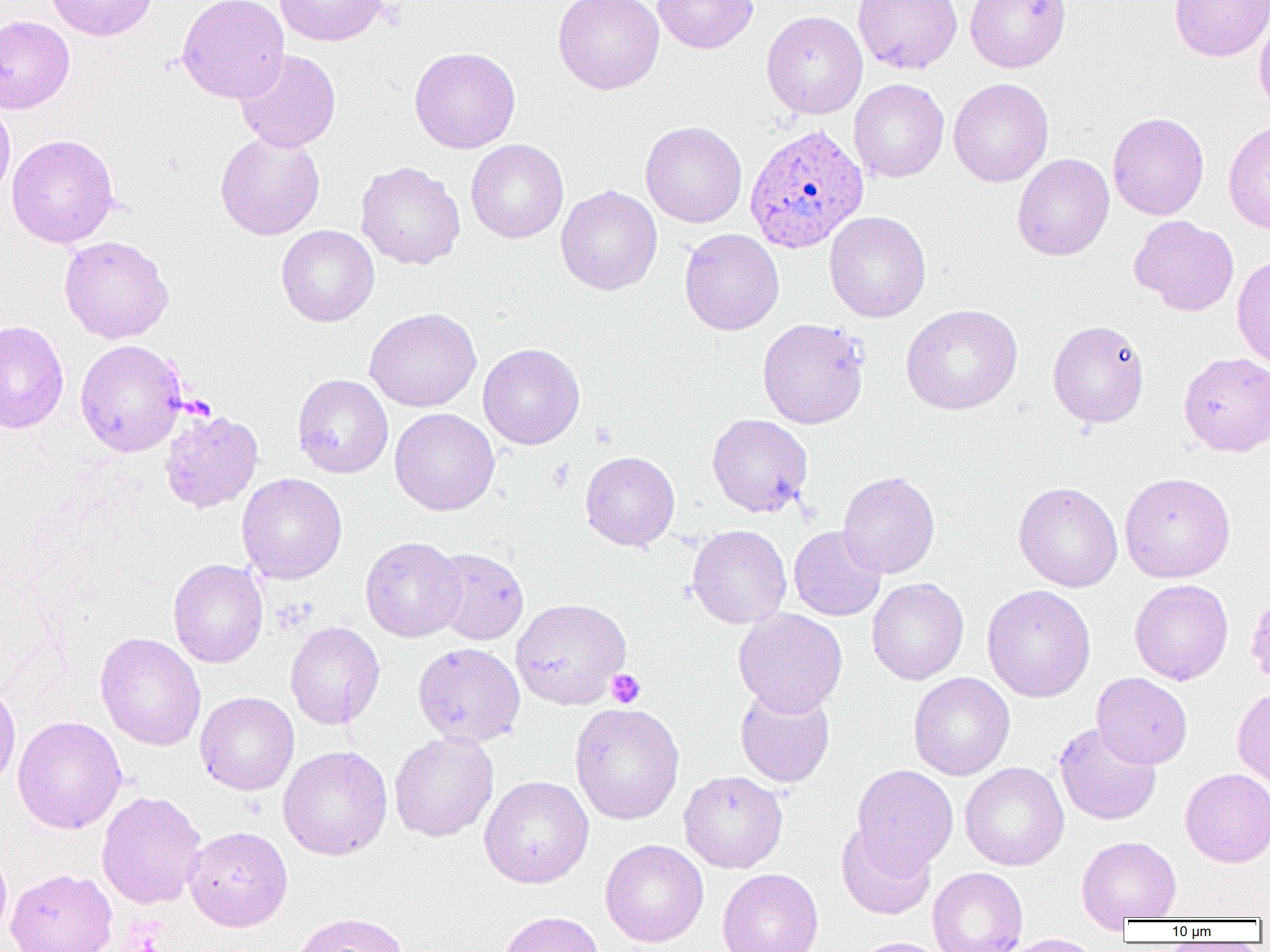
Summary:
  - Coordinate format: approximate bounding boxes as (x1, y1, x2, y2) in pixels
  - Plasmodium ovale-infected red blood cell locations: (743, 123, 869, 253)
  - Uninfected red blood cell locations: (45, 0, 158, 41), (177, 0, 290, 103), (275, 0, 387, 47), (553, 0, 664, 94), (652, 0, 758, 54), (853, 0, 962, 74), (964, 0, 1071, 72), (1169, 1, 1270, 62), (1254, 7, 1270, 118), (761, 10, 868, 118), (0, 15, 75, 113), (409, 46, 521, 153), (235, 49, 341, 152), (948, 77, 1054, 187), (849, 78, 949, 183), (0, 97, 15, 205), (1107, 112, 1209, 220), (1223, 120, 1270, 234), (640, 121, 747, 228), (215, 132, 325, 241), (7, 134, 119, 247), (466, 139, 568, 243), (1012, 153, 1114, 261), (355, 160, 465, 270), (556, 185, 662, 295), (824, 211, 931, 322), (1129, 215, 1239, 316), (276, 224, 379, 327), (679, 228, 784, 335), (59, 235, 174, 343), (1232, 254, 1270, 370), (900, 303, 1023, 414), (364, 307, 482, 412), (757, 317, 870, 429), (1047, 319, 1150, 428), (0, 320, 69, 433), (75, 339, 187, 457), (478, 343, 585, 449), (1179, 351, 1269, 456), (292, 374, 393, 478), (390, 407, 500, 515), (159, 408, 264, 514), (707, 413, 812, 517), (580, 451, 680, 551), (838, 470, 940, 579), (1119, 471, 1235, 582), (237, 473, 347, 584), (1013, 481, 1123, 592), (687, 524, 792, 629), (789, 526, 887, 621), (360, 535, 466, 642), (430, 547, 529, 645), (168, 558, 267, 668), (866, 577, 969, 685), (1129, 579, 1233, 685), (982, 584, 1096, 702), (1246, 590, 1270, 690), (510, 598, 631, 709), (733, 608, 847, 717), (285, 621, 385, 730), (95, 632, 206, 750), (412, 641, 526, 747), (908, 671, 1015, 780), (1091, 672, 1193, 769), (0, 682, 21, 792), (735, 685, 835, 787), (1232, 687, 1270, 788), (195, 691, 299, 795), (569, 702, 685, 825), (12, 715, 127, 834), (1053, 722, 1162, 825), (389, 731, 499, 842), (278, 745, 392, 860), (960, 762, 1069, 870), (851, 764, 958, 873), (1180, 768, 1270, 867), (679, 770, 788, 873), (479, 775, 594, 888), (96, 790, 207, 909), (836, 823, 936, 920), (184, 825, 293, 932), (1077, 835, 1182, 925), (600, 839, 709, 947), (0, 841, 12, 943), (927, 866, 1028, 952), (5, 867, 118, 952), (717, 868, 824, 952), (496, 910, 604, 952), (289, 911, 411, 952), (999, 934, 1106, 952), (849, 937, 952, 952)
  - Platelet locations: (607, 669, 645, 708)
  - Slide-level diagnosis: Plasmodium ovale
  - Magnification: 1000x
  - Field of view: single
  - Image size: 1270×952 pixels
  - Preparation: thin blood smear
  - Modality: optical microscopy